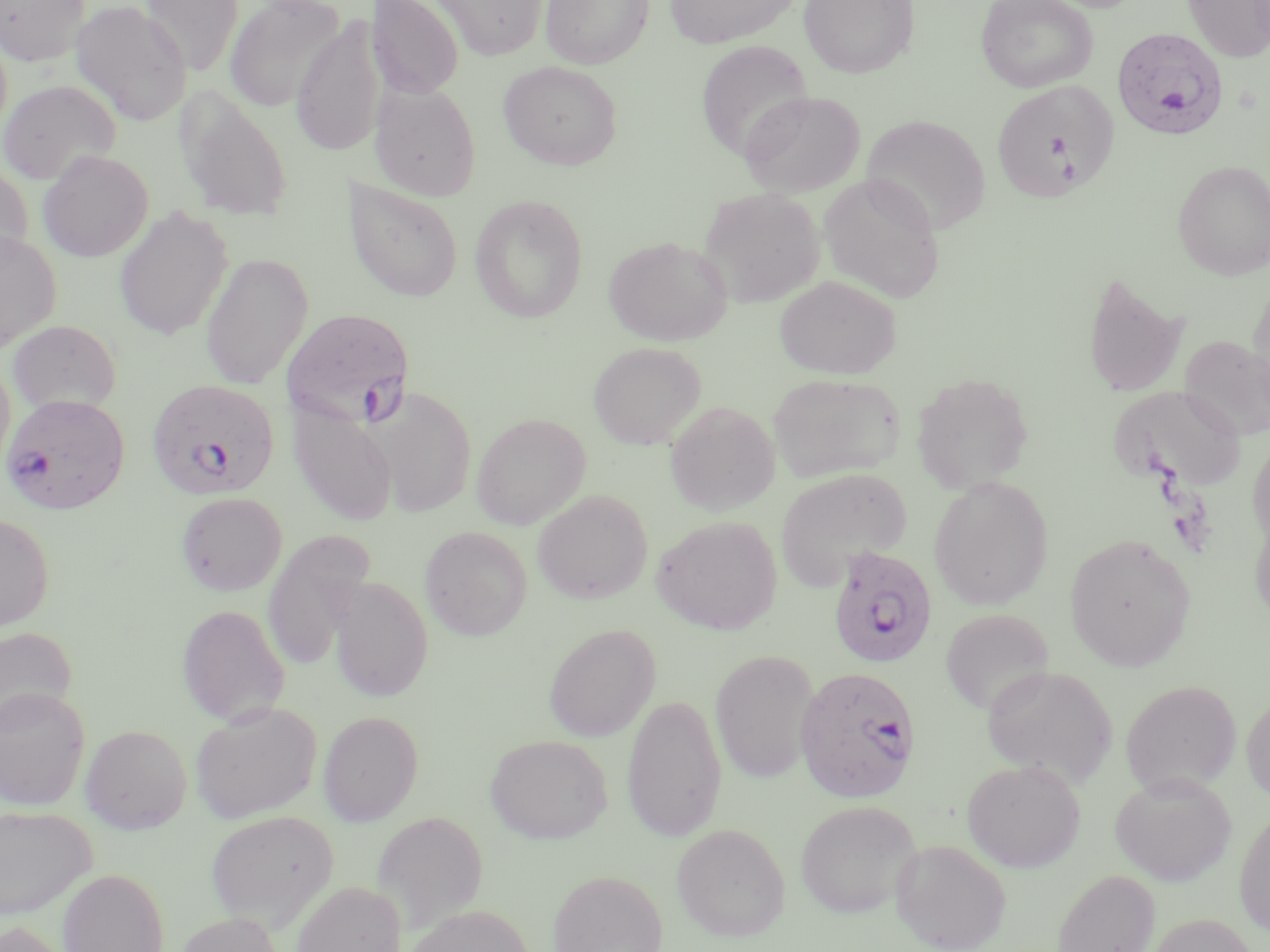
slide-level diagnosis = Plasmodium falciparum
modality = light microscopy
uninfected red blood cell locations = approximate bounding boxes as named x1/y1/x2/y2 corners in pixels: (x1=1, y1=0, x2=90, y2=66), (x1=142, y1=0, x2=243, y2=76), (x1=225, y1=0, x2=345, y2=113), (x1=366, y1=0, x2=464, y2=100), (x1=431, y1=0, x2=549, y2=60), (x1=541, y1=0, x2=653, y2=69), (x1=663, y1=0, x2=800, y2=48), (x1=798, y1=0, x2=919, y2=79), (x1=975, y1=0, x2=1098, y2=92), (x1=1183, y1=0, x2=1270, y2=62), (x1=70, y1=1, x2=192, y2=127), (x1=291, y1=15, x2=387, y2=158), (x1=0, y1=26, x2=13, y2=145), (x1=695, y1=40, x2=814, y2=161), (x1=498, y1=61, x2=623, y2=170), (x1=991, y1=79, x2=1118, y2=202), (x1=0, y1=80, x2=121, y2=185), (x1=370, y1=82, x2=481, y2=201), (x1=176, y1=90, x2=294, y2=221), (x1=739, y1=91, x2=865, y2=197), (x1=860, y1=114, x2=991, y2=236), (x1=38, y1=150, x2=153, y2=262), (x1=1172, y1=159, x2=1270, y2=280), (x1=0, y1=163, x2=33, y2=272), (x1=819, y1=174, x2=946, y2=302), (x1=343, y1=177, x2=464, y2=303), (x1=699, y1=188, x2=825, y2=308), (x1=469, y1=194, x2=589, y2=323), (x1=114, y1=207, x2=234, y2=341), (x1=0, y1=231, x2=61, y2=353), (x1=603, y1=235, x2=733, y2=346), (x1=200, y1=252, x2=314, y2=390), (x1=1082, y1=269, x2=1189, y2=399), (x1=774, y1=276, x2=902, y2=380), (x1=1248, y1=277, x2=1270, y2=410), (x1=7, y1=320, x2=121, y2=417), (x1=1179, y1=335, x2=1270, y2=440), (x1=588, y1=342, x2=705, y2=450), (x1=0, y1=354, x2=15, y2=481), (x1=910, y1=372, x2=1034, y2=494), (x1=767, y1=373, x2=905, y2=484), (x1=1110, y1=385, x2=1246, y2=492), (x1=369, y1=386, x2=477, y2=519), (x1=288, y1=400, x2=399, y2=527), (x1=665, y1=401, x2=781, y2=516), (x1=471, y1=413, x2=591, y2=530), (x1=1248, y1=438, x2=1270, y2=551), (x1=775, y1=467, x2=912, y2=589), (x1=928, y1=476, x2=1054, y2=610), (x1=532, y1=489, x2=653, y2=604), (x1=175, y1=491, x2=288, y2=597), (x1=1250, y1=507, x2=1270, y2=628), (x1=0, y1=512, x2=55, y2=631), (x1=652, y1=516, x2=782, y2=636), (x1=419, y1=526, x2=533, y2=641), (x1=262, y1=530, x2=377, y2=672), (x1=1065, y1=533, x2=1197, y2=670), (x1=327, y1=575, x2=434, y2=703), (x1=176, y1=604, x2=290, y2=727), (x1=940, y1=609, x2=1054, y2=716), (x1=543, y1=624, x2=661, y2=742), (x1=0, y1=625, x2=78, y2=731), (x1=711, y1=649, x2=820, y2=783), (x1=982, y1=664, x2=1119, y2=788), (x1=1120, y1=680, x2=1241, y2=796), (x1=0, y1=686, x2=90, y2=810), (x1=1241, y1=690, x2=1270, y2=805), (x1=622, y1=693, x2=727, y2=843), (x1=189, y1=702, x2=321, y2=824), (x1=318, y1=710, x2=424, y2=825), (x1=80, y1=724, x2=192, y2=834), (x1=485, y1=734, x2=612, y2=844), (x1=961, y1=759, x2=1085, y2=872), (x1=1110, y1=771, x2=1237, y2=886), (x1=795, y1=800, x2=921, y2=919), (x1=0, y1=805, x2=96, y2=919), (x1=1234, y1=808, x2=1270, y2=936), (x1=205, y1=810, x2=338, y2=929), (x1=372, y1=811, x2=489, y2=931), (x1=672, y1=823, x2=790, y2=941), (x1=891, y1=838, x2=1012, y2=952), (x1=58, y1=868, x2=169, y2=952), (x1=1052, y1=868, x2=1161, y2=952), (x1=548, y1=869, x2=668, y2=952), (x1=292, y1=881, x2=406, y2=952), (x1=405, y1=903, x2=534, y2=952), (x1=174, y1=912, x2=285, y2=952), (x1=1146, y1=913, x2=1258, y2=952), (x1=0, y1=920, x2=72, y2=952)
Plasmodium falciparum-infected red blood cell locations = approximate bounding boxes as named x1/y1/x2/y2 corners in pixels: (x1=1112, y1=27, x2=1230, y2=140), (x1=281, y1=309, x2=414, y2=428), (x1=146, y1=379, x2=281, y2=500), (x1=1, y1=393, x2=130, y2=515), (x1=827, y1=546, x2=939, y2=670), (x1=795, y1=665, x2=921, y2=803)
image size = 1270×952 pixels
field of view = single
magnification = 1000x
preparation = thin blood film
stain = May-Grünwald-Giemsa